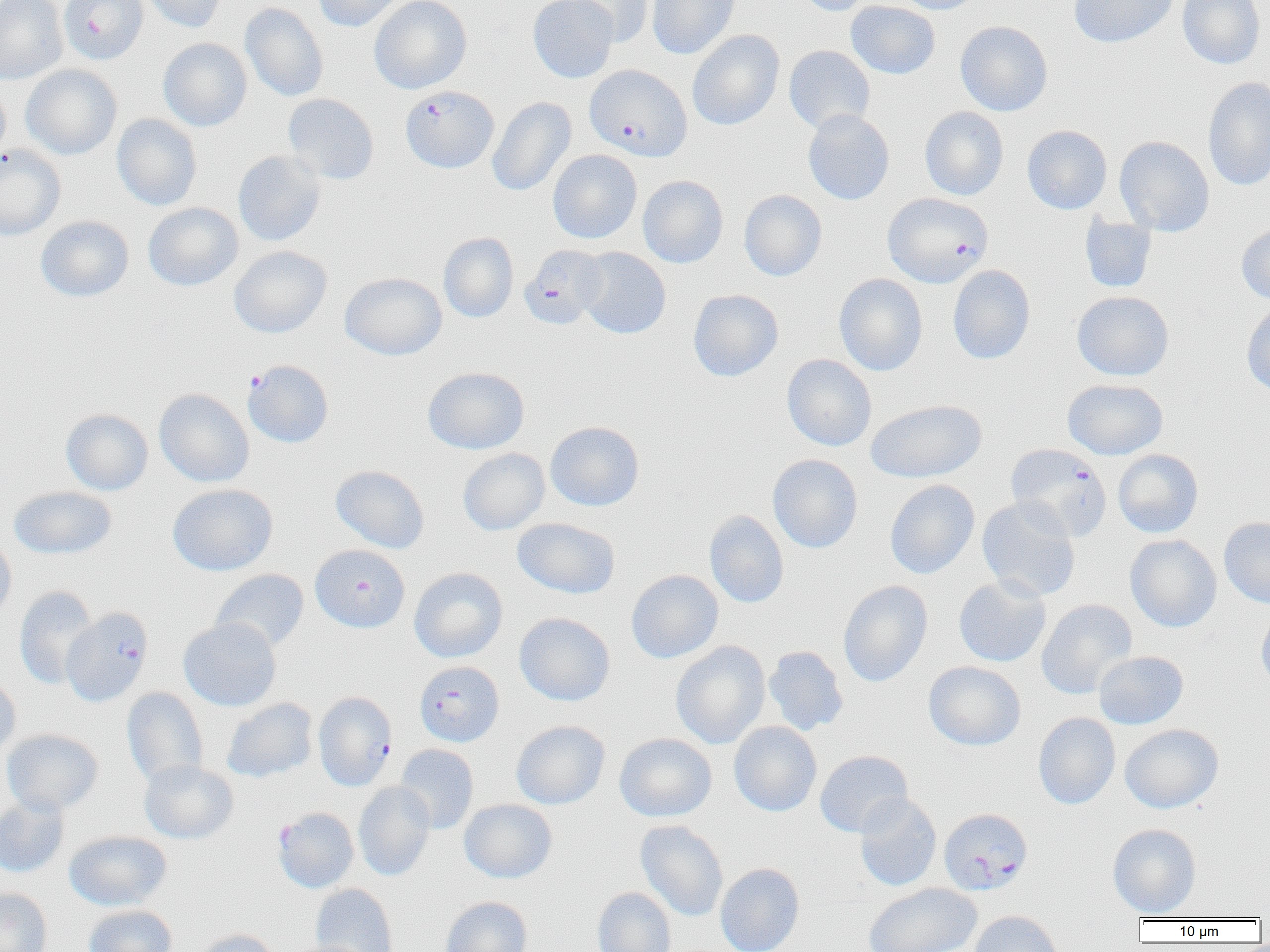
Summary:
  - Coordinate format: approximate bounding boxes as [x1, y1, x2, y2] in pixels
  - Uninfected red blood cell locations: [0, 0, 68, 83], [137, 0, 229, 33], [313, 0, 409, 31], [369, 0, 472, 94], [528, 0, 618, 83], [647, 0, 740, 59], [793, 0, 877, 16], [890, 0, 985, 14], [1069, 0, 1179, 48], [1177, 0, 1265, 69], [563, 1, 653, 46], [845, 1, 940, 79], [240, 2, 328, 101], [955, 21, 1053, 116], [687, 30, 784, 131], [158, 38, 252, 131], [783, 45, 875, 134], [20, 64, 122, 159], [1203, 76, 1270, 191], [0, 79, 10, 167], [283, 93, 379, 185], [487, 96, 576, 196], [920, 107, 1009, 200], [803, 109, 895, 205], [112, 114, 202, 211], [1022, 125, 1112, 214], [1020, 131, 1215, 222], [1115, 136, 1214, 236], [0, 145, 65, 241], [232, 150, 326, 246], [547, 150, 642, 244], [637, 175, 729, 268], [739, 190, 827, 281], [143, 202, 243, 291], [1079, 213, 1157, 293], [35, 215, 134, 302], [1236, 224, 1270, 305], [438, 232, 519, 323], [229, 245, 332, 338], [576, 247, 671, 339], [947, 265, 1035, 364], [339, 272, 446, 360], [834, 273, 928, 376], [688, 289, 784, 382], [1072, 291, 1174, 381], [1241, 302, 1270, 396], [781, 354, 877, 451], [423, 366, 530, 454], [1062, 378, 1168, 459], [154, 388, 254, 487], [866, 400, 987, 483], [60, 408, 153, 495], [545, 421, 644, 511], [458, 448, 549, 535], [1113, 449, 1203, 538], [767, 454, 863, 553], [330, 465, 429, 554], [885, 479, 980, 579], [168, 484, 278, 576], [8, 486, 117, 559], [977, 497, 1081, 601], [704, 510, 789, 608], [1219, 517, 1270, 607], [512, 518, 621, 599], [0, 534, 16, 622], [1125, 534, 1222, 632], [409, 567, 508, 662], [210, 569, 309, 653], [626, 569, 723, 663], [953, 575, 1051, 668], [838, 580, 933, 687], [14, 586, 98, 688], [1036, 599, 1137, 699], [1256, 604, 1270, 692], [514, 612, 616, 706], [178, 618, 281, 711], [671, 640, 770, 749], [764, 645, 849, 736], [1093, 651, 1188, 729], [924, 661, 1026, 751], [0, 673, 21, 759], [122, 687, 209, 786], [221, 698, 318, 783], [1033, 712, 1120, 809], [511, 720, 610, 809], [729, 721, 822, 816], [1119, 724, 1223, 813], [2, 729, 103, 816], [614, 733, 717, 822], [394, 744, 479, 834], [815, 750, 913, 838], [139, 760, 239, 844], [353, 781, 435, 881], [854, 793, 942, 891], [0, 795, 70, 878], [459, 799, 557, 883], [635, 820, 729, 921], [1107, 823, 1201, 918], [64, 831, 171, 911], [715, 863, 804, 952], [864, 882, 982, 952], [310, 884, 398, 951], [592, 887, 676, 952], [0, 888, 52, 952], [440, 896, 533, 952], [82, 905, 177, 952], [968, 911, 1063, 952], [194, 928, 281, 952]
  - Plasmodium falciparum-infected red blood cell locations: [58, 0, 148, 65], [584, 64, 692, 161], [400, 86, 499, 173], [883, 193, 993, 288], [520, 244, 608, 330], [243, 360, 333, 448], [1006, 443, 1112, 541], [310, 544, 410, 632], [61, 607, 153, 707], [419, 664, 508, 750], [313, 691, 397, 790], [273, 807, 359, 893], [939, 808, 1033, 895]
  - Slide-level diagnosis: Plasmodium falciparum
  - Field of view: one of a larger specimen
  - Magnification: 1000x
  - Modality: light microscopy
  - Image size: 1270×952 pixels
  - Preparation: thin blood film